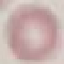

Summary:
  - Malaria status: uninfected
  - Preparation: thin smear
  - Stain: Giemsa
  - Capture: smartphone through the microscope eyepiece
  - Image type: automatically extracted cell patch, resized to 64 × 64 pixels